Assess this cell for malaria.
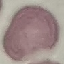

Uninfected.

Summary:
  - Stain: Giemsa
  - Capture: smartphone camera at the microscope eyepiece
  - Preparation: thin blood film
  - Image type: cell patch, automatically extracted from a larger field of view and resized to 64 × 64 pixels